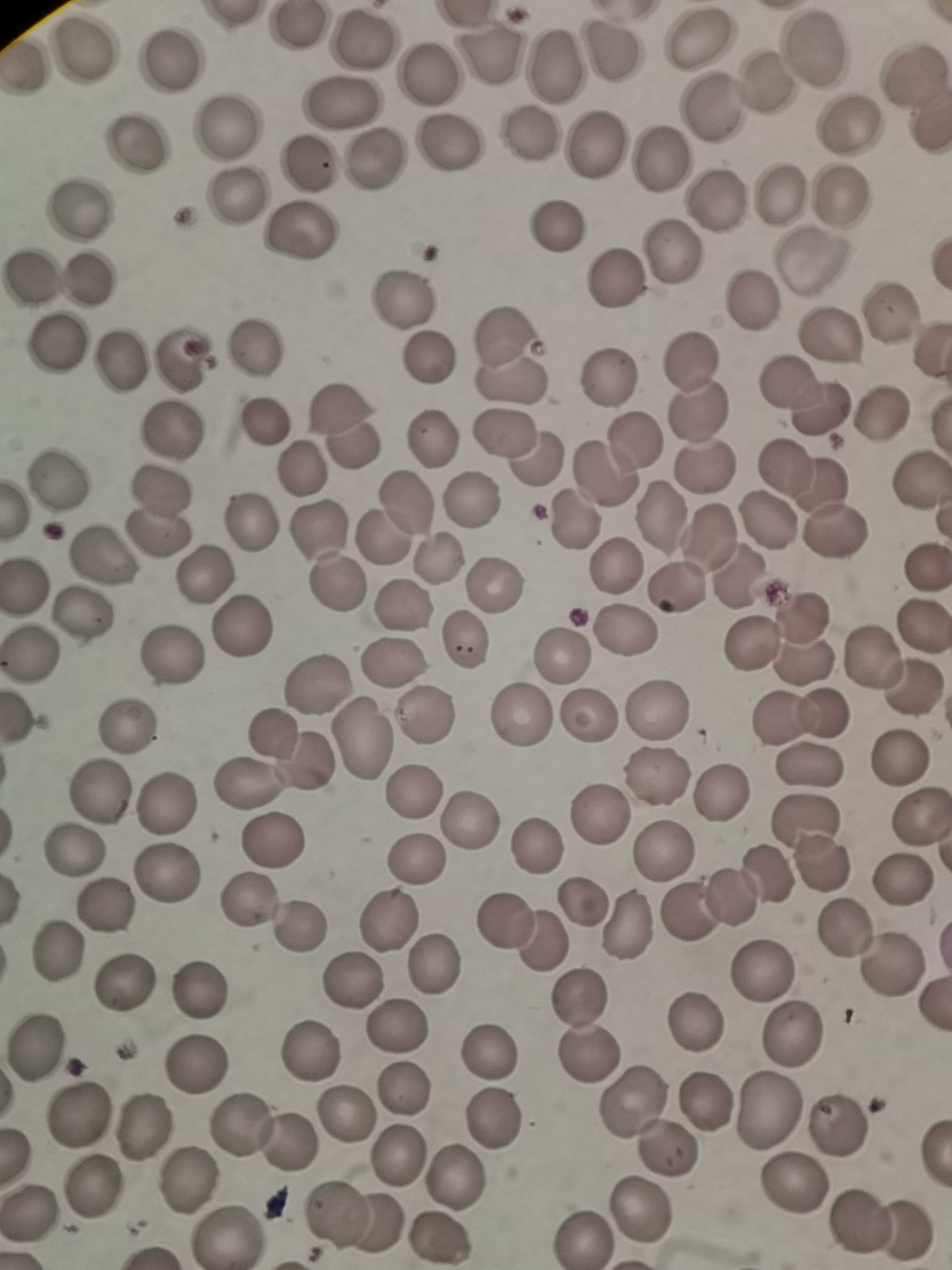
Approximate centers as [x, y] in pixels. Cell locations: [695, 38], [362, 40], [814, 47], [78, 50], [486, 53], [614, 54], [170, 61], [551, 65], [912, 74], [426, 75], [766, 79], [341, 100], [711, 107], [850, 127], [227, 129], [525, 134], [447, 142], [593, 143], [136, 150], [656, 158], [375, 159], [305, 164], [842, 194], [779, 197], [234, 198], [712, 202], [79, 210], [555, 224], [305, 234], [673, 251], [31, 279], [89, 279], [614, 279], [749, 298], [401, 300], [888, 312], [830, 335], [500, 338], [53, 344], [253, 350], [180, 359], [425, 359], [687, 361], [120, 364], [607, 376], [511, 377], [803, 397], [345, 409], [880, 411], [699, 413], [266, 416], [173, 429], [504, 434], [431, 439], [354, 445], [616, 457], [536, 459], [707, 464], [804, 472], [61, 481], [919, 481], [470, 500], [160, 514], [660, 514], [393, 519], [250, 521], [768, 521], [570, 523], [835, 531], [318, 532], [102, 557], [727, 558], [438, 561], [617, 564], [922, 567], [205, 578], [26, 582], [338, 587], [494, 587], [677, 587], [402, 607], [83, 612], [922, 621], [241, 626], [625, 632], [806, 638], [754, 642], [467, 643], [873, 654], [29, 655], [560, 656], [173, 658], [393, 662], [317, 681], [914, 690], [658, 709], [587, 714], [518, 715], [427, 716], [800, 717], [126, 727], [361, 736], [271, 759], [898, 759], [806, 764], [655, 774], [411, 790], [101, 791], [720, 794], [168, 802], [596, 814], [921, 820], [470, 821], [270, 841], [808, 841], [536, 844], [663, 849], [75, 852], [417, 860], [166, 871], [904, 879], [730, 892], [585, 897], [246, 898], [108, 906], [629, 921], [388, 922], [502, 922], [299, 929], [846, 931], [541, 938], [55, 953], [437, 965], [892, 966], [761, 970], [352, 982], [122, 984], [197, 991], [584, 998], [693, 1025], [396, 1027], [793, 1037], [39, 1047], [485, 1048], [588, 1048], [311, 1051], [196, 1058], [405, 1089], [631, 1100], [707, 1102], [345, 1113], [769, 1113], [495, 1114], [79, 1116], [242, 1121], [839, 1124], [140, 1127], [287, 1143], [665, 1149], [396, 1156], [185, 1178], [456, 1179], [794, 1186], [87, 1192], [28, 1210], [642, 1210], [353, 1218], [861, 1221], [230, 1235], [579, 1237], [438, 1241]. Photographed with a smartphone camera at the microscope eyepiece. Image is 952×1270 pixels. Single field of view. Thin smear of blood. Giemsa stain.